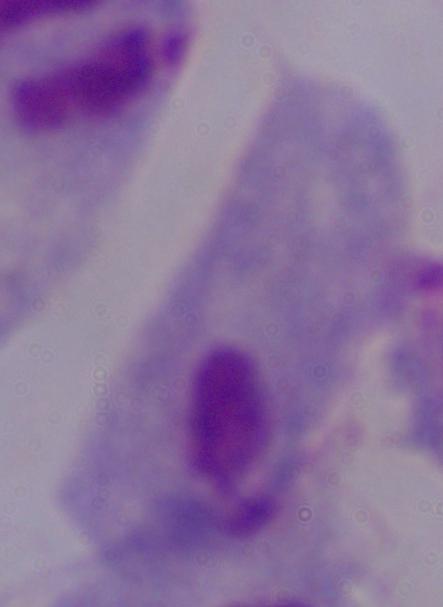
A trichomonad is shown. 1000x magnification. Photomicrograph.